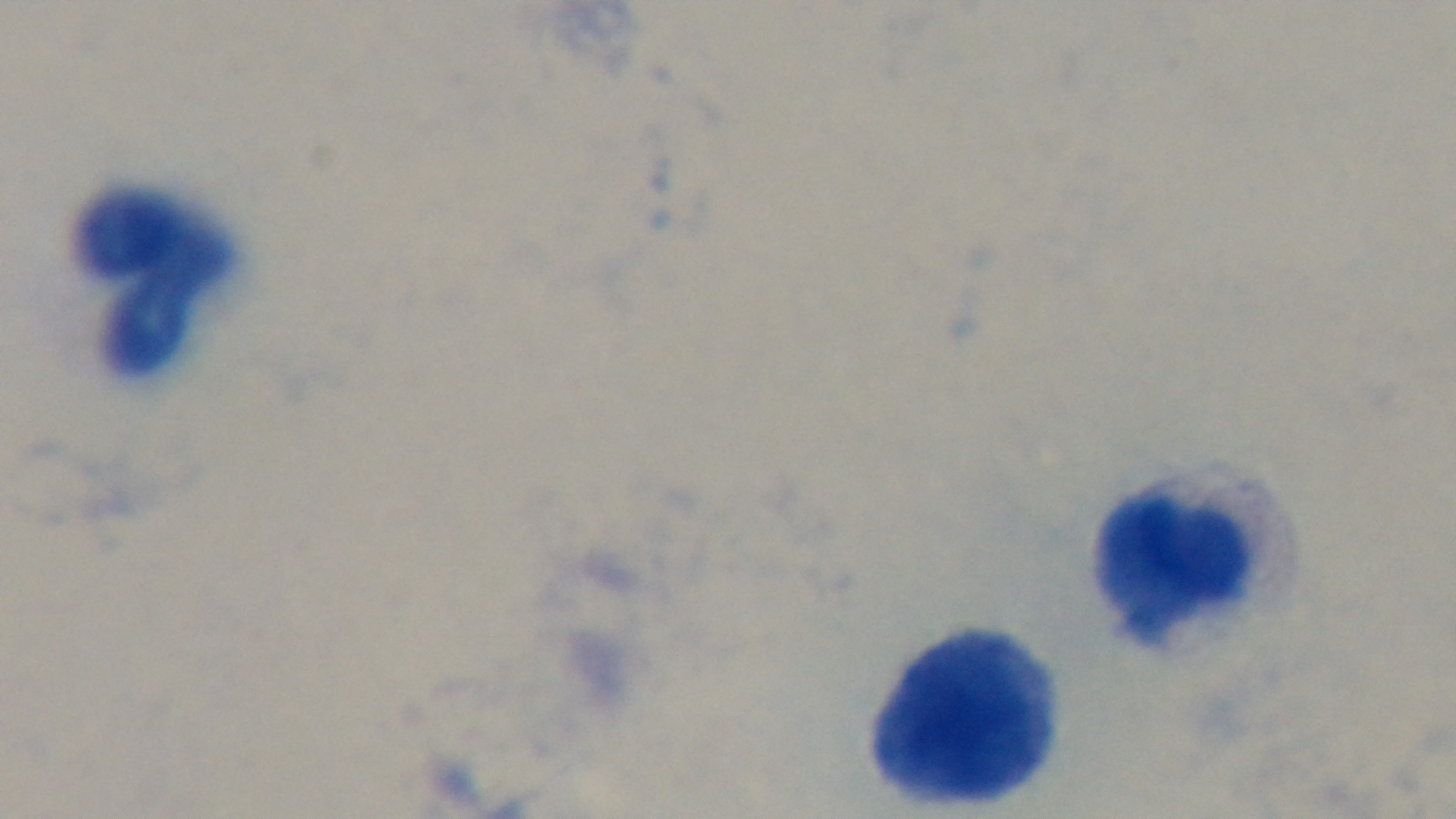

Summary:
  - Malaria status: negative
  - Modality: light microscopy
  - Preparation: thick smear
  - Stain: Giemsa
  - Field of view: single
  - Capture: mounted 4K digital camera
  - Objective: 100x oil immersion